Outline each blood parasite and name the species.
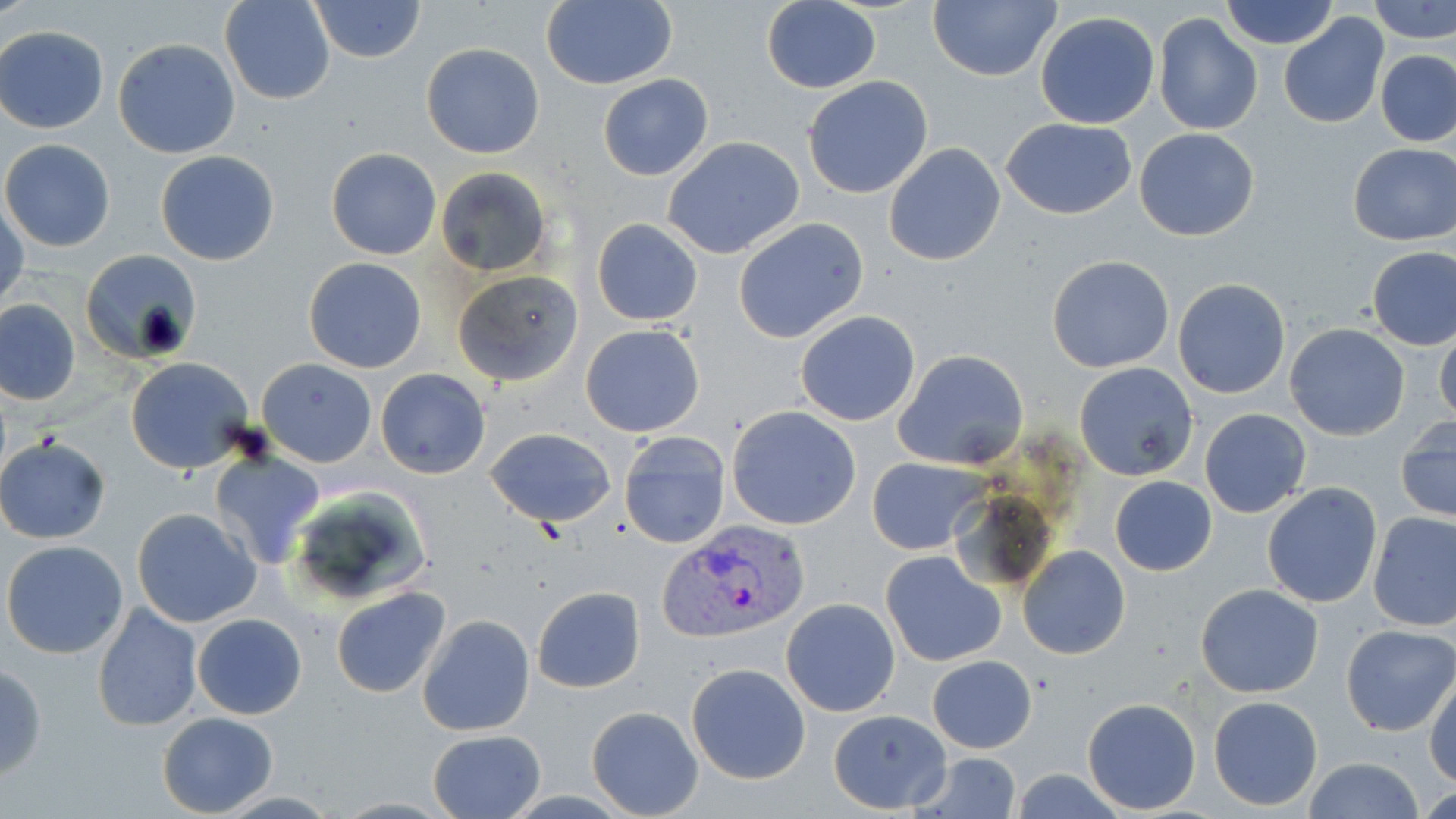
Approximate bounding boxes as named x1/y1/x2/y2 corners in pixels.
Plasmodium vivax-infected red blood cells: (x1=660, y1=520, x2=810, y2=645).
No Plasmodium falciparum, Plasmodium ovale, Plasmodium malariae, Babesia divergens, or Trypanosoma brucei observed.

{
  "slide_level_diagnosis": "Plasmodium vivax",
  "modality": "optical microscopy",
  "image_size": "1456×819 pixels",
  "stain": "May-Grünwald-Giemsa",
  "magnification": "1000x",
  "preparation": "thin blood film",
  "field_of_view": "one of a larger specimen",
  "uninfected_red_blood_cell_locations": "approximate bounding boxes as named x1/y1/x2/y2 corners in pixels: (x1=220, y1=0, x2=335, y2=104), (x1=312, y1=0, x2=425, y2=63), (x1=540, y1=0, x2=678, y2=89), (x1=1219, y1=0, x2=1339, y2=50), (x1=1370, y1=0, x2=1456, y2=42), (x1=759, y1=1, x2=881, y2=92), (x1=928, y1=1, x2=1061, y2=82), (x1=1035, y1=12, x2=1161, y2=129), (x1=1278, y1=12, x2=1389, y2=128), (x1=1153, y1=13, x2=1262, y2=136), (x1=1, y1=28, x2=108, y2=133), (x1=113, y1=38, x2=241, y2=158), (x1=421, y1=43, x2=546, y2=160), (x1=1377, y1=51, x2=1455, y2=145), (x1=598, y1=74, x2=713, y2=182), (x1=802, y1=77, x2=934, y2=200), (x1=1002, y1=118, x2=1136, y2=219), (x1=1134, y1=127, x2=1259, y2=241), (x1=662, y1=136, x2=805, y2=259), (x1=1, y1=138, x2=116, y2=252), (x1=882, y1=142, x2=1006, y2=266), (x1=1349, y1=142, x2=1455, y2=245), (x1=326, y1=148, x2=443, y2=260), (x1=154, y1=150, x2=280, y2=266), (x1=435, y1=166, x2=552, y2=277), (x1=1, y1=198, x2=26, y2=311), (x1=591, y1=218, x2=704, y2=326), (x1=733, y1=218, x2=869, y2=344), (x1=1368, y1=247, x2=1456, y2=349), (x1=78, y1=248, x2=202, y2=365), (x1=1046, y1=255, x2=1175, y2=373), (x1=303, y1=256, x2=427, y2=373), (x1=452, y1=269, x2=584, y2=386), (x1=1173, y1=278, x2=1292, y2=399), (x1=1, y1=299, x2=79, y2=405), (x1=794, y1=311, x2=920, y2=427), (x1=1433, y1=322, x2=1456, y2=427), (x1=1284, y1=323, x2=1411, y2=440), (x1=580, y1=325, x2=705, y2=437), (x1=895, y1=350, x2=1029, y2=470), (x1=124, y1=356, x2=256, y2=475), (x1=255, y1=357, x2=376, y2=466), (x1=1074, y1=362, x2=1198, y2=481), (x1=375, y1=368, x2=491, y2=479), (x1=727, y1=406, x2=862, y2=531), (x1=1200, y1=408, x2=1312, y2=519), (x1=1396, y1=418, x2=1455, y2=526), (x1=485, y1=427, x2=617, y2=528), (x1=619, y1=431, x2=731, y2=548), (x1=0, y1=435, x2=110, y2=544), (x1=208, y1=449, x2=325, y2=569), (x1=866, y1=457, x2=984, y2=554), (x1=1109, y1=475, x2=1217, y2=576), (x1=1262, y1=483, x2=1382, y2=608), (x1=286, y1=484, x2=433, y2=607), (x1=131, y1=507, x2=261, y2=628), (x1=1368, y1=511, x2=1456, y2=632), (x1=2, y1=540, x2=130, y2=659), (x1=1017, y1=545, x2=1132, y2=660), (x1=880, y1=550, x2=1007, y2=668), (x1=1195, y1=584, x2=1324, y2=698), (x1=331, y1=585, x2=449, y2=698), (x1=531, y1=585, x2=645, y2=693), (x1=780, y1=598, x2=901, y2=717), (x1=91, y1=603, x2=203, y2=732), (x1=192, y1=613, x2=308, y2=720), (x1=418, y1=614, x2=535, y2=736), (x1=1342, y1=625, x2=1456, y2=737), (x1=927, y1=655, x2=1037, y2=754), (x1=685, y1=663, x2=812, y2=784), (x1=0, y1=664, x2=45, y2=782), (x1=1426, y1=671, x2=1456, y2=789), (x1=1209, y1=695, x2=1324, y2=809), (x1=1081, y1=697, x2=1201, y2=814), (x1=586, y1=705, x2=705, y2=818), (x1=829, y1=709, x2=952, y2=814), (x1=156, y1=712, x2=278, y2=817), (x1=427, y1=730, x2=547, y2=818), (x1=914, y1=751, x2=1024, y2=819), (x1=1303, y1=757, x2=1425, y2=819), (x1=1011, y1=767, x2=1129, y2=819)"
}